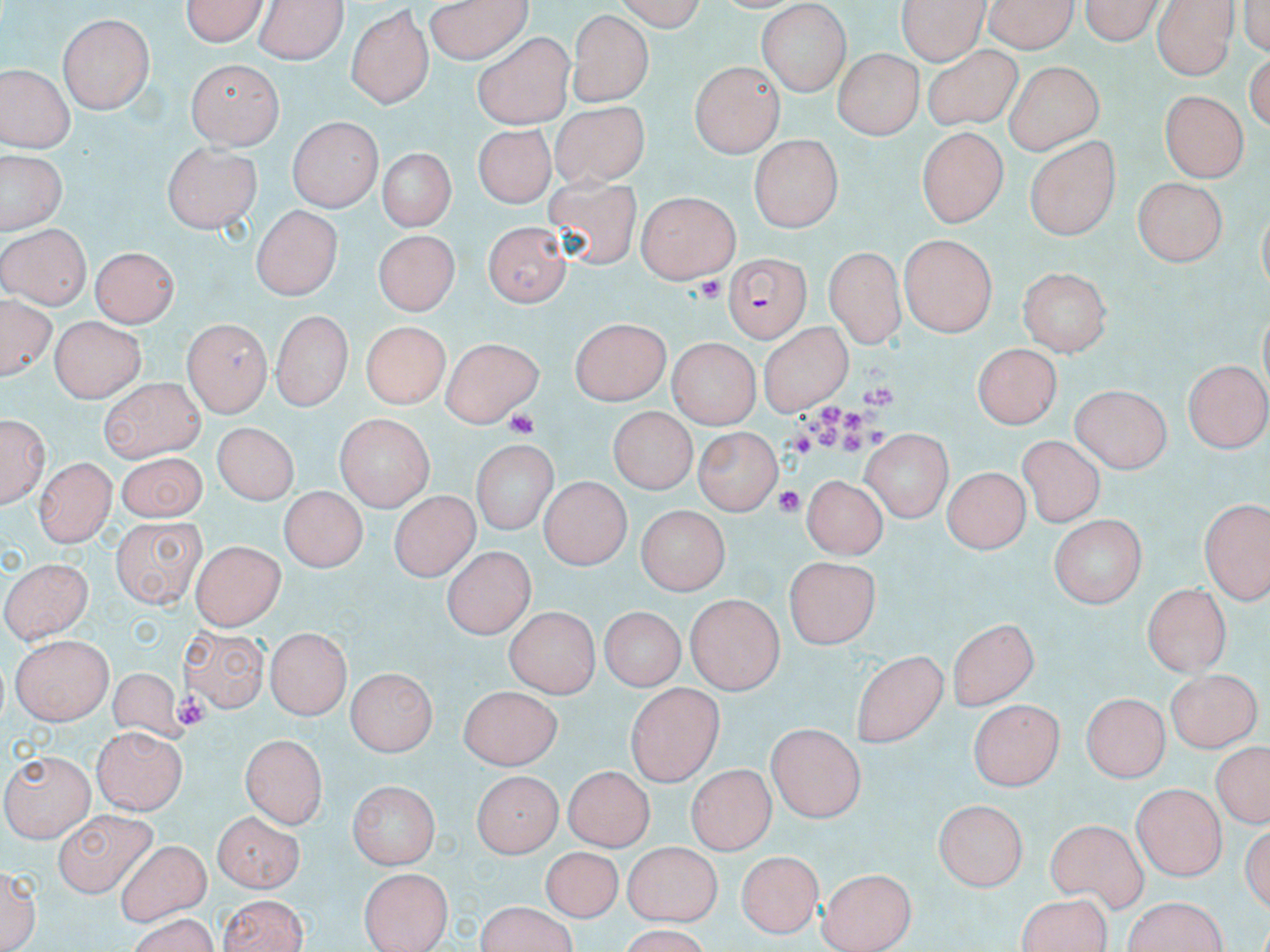
Approximate bounding boxes as (x1,y1)-(x2,y2) corner pairs in pixels. Uninfected red blood cell locations: (180,0)-(269,47), (257,0)-(345,65), (607,0)-(708,29), (895,0)-(990,60), (983,0)-(1081,53), (1077,0)-(1167,46), (426,1)-(532,63), (1151,3)-(1234,80), (755,5)-(846,94), (345,7)-(434,108), (902,9)-(1007,104), (568,12)-(654,108), (58,13)-(153,114), (473,34)-(574,129), (922,45)-(1022,128), (832,51)-(923,136), (188,60)-(280,149), (691,62)-(783,159), (1002,63)-(1100,155), (0,66)-(71,152), (1160,91)-(1245,182), (550,104)-(651,201), (289,117)-(382,211), (471,126)-(552,208), (916,128)-(1007,228), (748,136)-(842,234), (1026,136)-(1122,238), (163,139)-(262,232), (377,148)-(455,232), (1,151)-(67,234), (543,178)-(641,282), (1134,178)-(1226,267), (634,192)-(742,280), (250,208)-(341,301), (482,222)-(569,306), (0,226)-(88,309), (373,232)-(456,317), (900,234)-(999,335), (92,246)-(179,328), (824,246)-(901,351), (1021,265)-(1112,354), (1,300)-(53,387), (271,308)-(351,413), (47,315)-(145,401), (571,318)-(672,407), (182,321)-(270,416), (758,321)-(852,416), (358,323)-(453,406), (443,337)-(546,428), (670,338)-(759,427), (972,342)-(1066,424), (1184,358)-(1270,450), (98,377)-(205,460), (1067,386)-(1172,471), (607,410)-(693,493), (2,413)-(47,509), (331,415)-(435,509), (210,424)-(298,509), (693,428)-(780,518), (863,428)-(952,521), (1018,436)-(1100,527), (472,438)-(554,538), (114,449)-(206,521), (35,456)-(115,546), (940,469)-(1029,553), (802,476)-(885,558), (541,478)-(628,569), (278,487)-(365,573), (390,490)-(475,582), (1200,501)-(1267,604), (638,508)-(727,595), (110,514)-(201,608), (1046,514)-(1146,608), (193,541)-(282,630), (441,548)-(534,639), (5,556)-(96,643), (785,558)-(882,647), (1143,583)-(1230,678), (685,597)-(781,694), (597,607)-(687,691), (503,608)-(598,697), (947,620)-(1039,710), (179,624)-(270,711), (263,629)-(348,718), (10,635)-(113,723), (852,649)-(949,748), (348,667)-(434,758), (1167,669)-(1257,752), (102,672)-(191,746), (459,684)-(563,771), (626,685)-(722,783), (1083,691)-(1168,784), (966,698)-(1064,790), (765,722)-(864,824), (92,727)-(186,814), (240,733)-(328,827), (1207,741)-(1268,830), (5,750)-(95,839), (566,764)-(655,852), (686,766)-(777,852), (470,772)-(559,858), (350,780)-(441,868), (1131,785)-(1223,880), (934,801)-(1027,890), (211,811)-(303,890), (53,812)-(154,898), (1044,817)-(1149,911), (115,840)-(209,923), (625,842)-(719,926), (544,845)-(622,915), (740,849)-(822,938), (1,859)-(40,952), (359,864)-(453,952), (818,867)-(914,952), (216,893)-(310,951), (476,902)-(582,952). Plasmodium falciparum-infected red blood cell locations: (723,257)-(811,340). Platelet locations: (702,275)-(725,307), (863,387)-(893,406), (819,404)-(840,427), (505,409)-(541,440), (842,410)-(862,433), (815,428)-(841,449), (867,428)-(890,448), (791,432)-(812,456), (841,433)-(861,452), (775,488)-(805,513), (172,694)-(208,728). Slide-level diagnosis: Plasmodium falciparum. Light microscopy. Thin blood smear. 1000x magnification. May-Grünwald-Giemsa stain. Image is 1270×952 pixels. One field of a larger specimen.